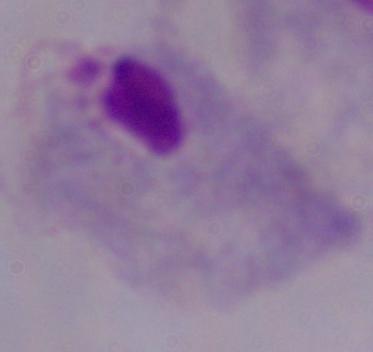 1000x magnification. A trichomonad is seen. Photomicrograph.